Locate every blood parasite and identify its species.
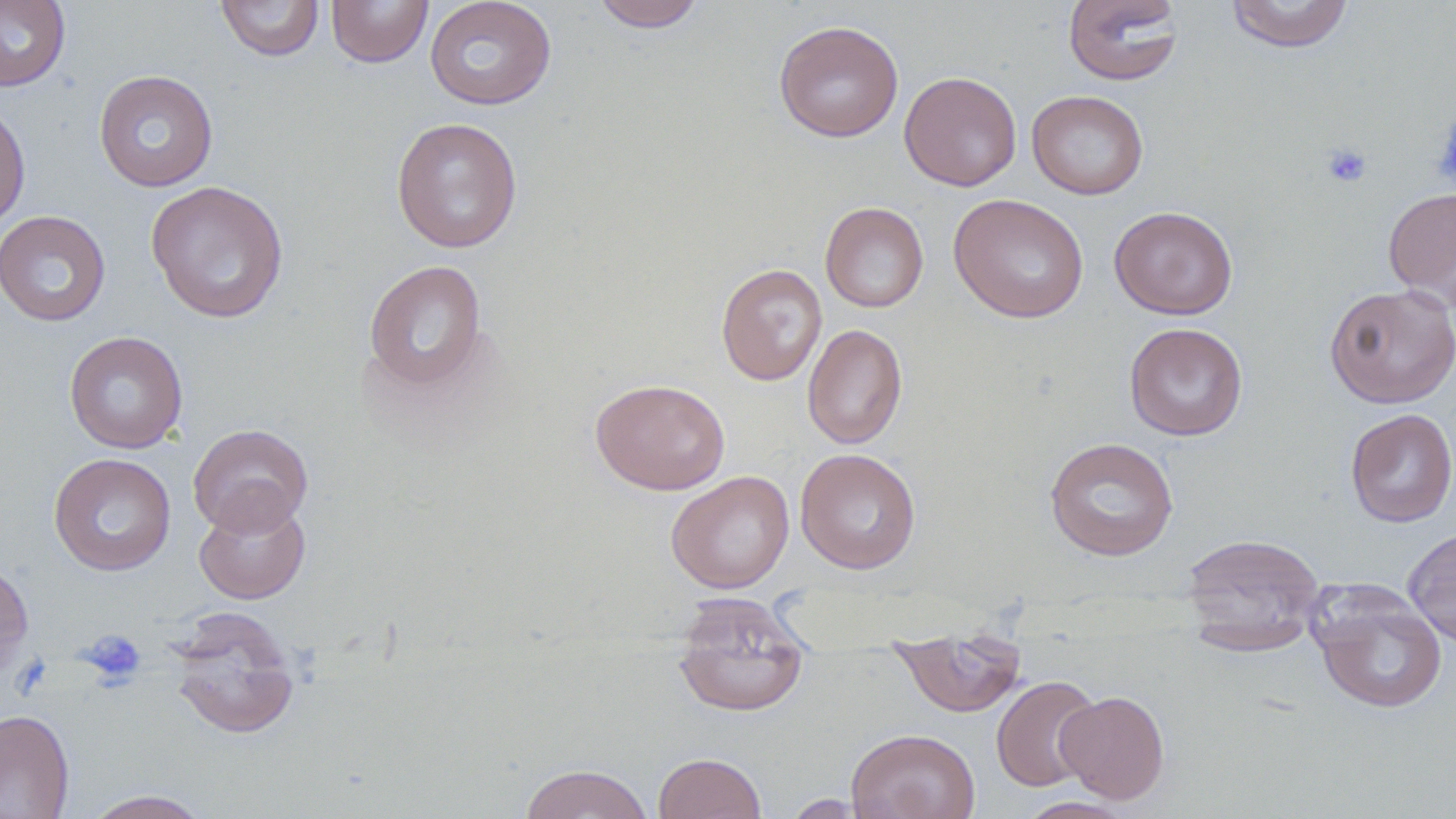
No blood parasites seen.

Approximate bounding boxes as named x1/y1/x2/y2 corners in pixels. Platelet locations: (x1=1433, y1=110, x2=1456, y2=189), (x1=1321, y1=142, x2=1373, y2=189), (x1=79, y1=628, x2=147, y2=690). Uninfected red blood cell locations: (x1=0, y1=0, x2=71, y2=92), (x1=215, y1=0, x2=324, y2=62), (x1=326, y1=0, x2=433, y2=67), (x1=425, y1=0, x2=557, y2=111), (x1=590, y1=0, x2=709, y2=32), (x1=1062, y1=0, x2=1184, y2=86), (x1=1225, y1=0, x2=1354, y2=53), (x1=774, y1=20, x2=904, y2=142), (x1=93, y1=69, x2=219, y2=192), (x1=899, y1=70, x2=1022, y2=191), (x1=1026, y1=90, x2=1149, y2=200), (x1=0, y1=101, x2=31, y2=230), (x1=391, y1=117, x2=523, y2=253), (x1=145, y1=180, x2=289, y2=323), (x1=1383, y1=187, x2=1456, y2=308), (x1=948, y1=193, x2=1089, y2=323), (x1=820, y1=201, x2=929, y2=313), (x1=1108, y1=205, x2=1238, y2=319), (x1=0, y1=210, x2=111, y2=326), (x1=363, y1=259, x2=488, y2=393), (x1=716, y1=264, x2=828, y2=386), (x1=1324, y1=284, x2=1456, y2=408), (x1=1123, y1=322, x2=1248, y2=441), (x1=802, y1=324, x2=907, y2=449), (x1=64, y1=331, x2=188, y2=454), (x1=590, y1=377, x2=730, y2=495), (x1=1345, y1=408, x2=1456, y2=527), (x1=188, y1=423, x2=314, y2=536), (x1=1044, y1=437, x2=1179, y2=562), (x1=795, y1=448, x2=921, y2=574), (x1=49, y1=452, x2=177, y2=576), (x1=666, y1=470, x2=794, y2=594), (x1=193, y1=497, x2=310, y2=604), (x1=1403, y1=527, x2=1456, y2=647), (x1=1181, y1=532, x2=1325, y2=649), (x1=0, y1=560, x2=34, y2=681), (x1=1311, y1=588, x2=1448, y2=714), (x1=671, y1=594, x2=812, y2=717), (x1=167, y1=608, x2=302, y2=741), (x1=891, y1=630, x2=1028, y2=718), (x1=991, y1=675, x2=1102, y2=792), (x1=1055, y1=690, x2=1170, y2=804), (x1=0, y1=710, x2=74, y2=819), (x1=846, y1=728, x2=980, y2=819), (x1=652, y1=752, x2=767, y2=819), (x1=518, y1=763, x2=654, y2=819), (x1=82, y1=789, x2=214, y2=818), (x1=782, y1=793, x2=872, y2=818), (x1=1014, y1=797, x2=1137, y2=819). Slide-level diagnosis: no evidence of blood parasites. Single field of view. May-Grünwald-Giemsa stain. Thin blood smear. Image is 1456×819 pixels. Light microscopy. 1000x magnification.